Comment on the morphology of the red blood cells.
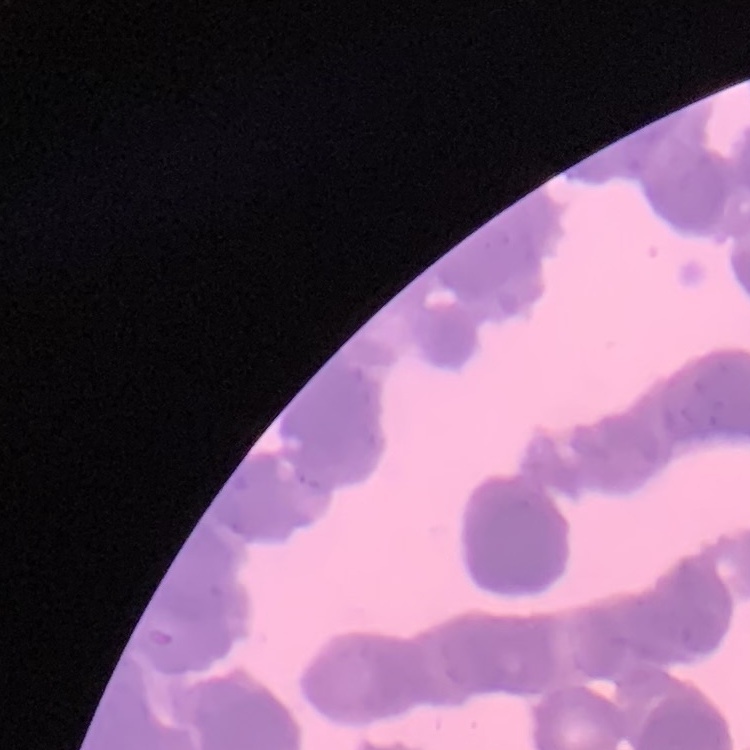

Rouleaux formation.

stain = Field's or Giemsa
image type = square crop of a larger photomicrograph
preparation = thin blood smear